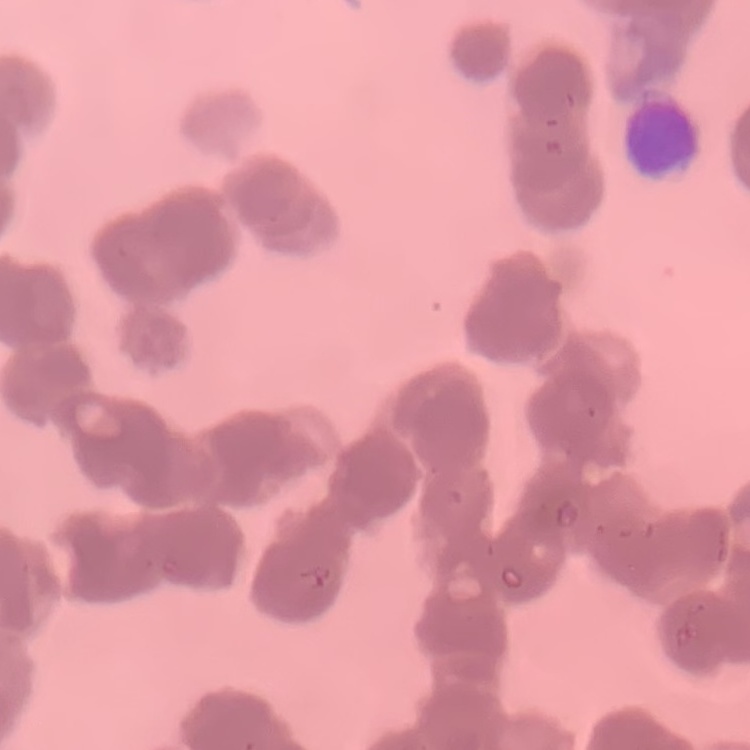
{
  "erythrocyte_morphology": "rouleaux formation",
  "image_type": "one tile cut from a larger photomicrograph",
  "stain": "Field's or Giemsa",
  "preparation": "thin blood film"
}